Assess this cell for malaria.
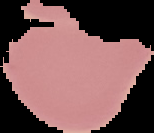
It is uninfected.

Summary:
  - Preparation: thin blood smear
  - Image size: 154×133 pixels
  - Image type: segmented cell region with the area outside set to black